Point out every malaria parasite and every leukocyte.
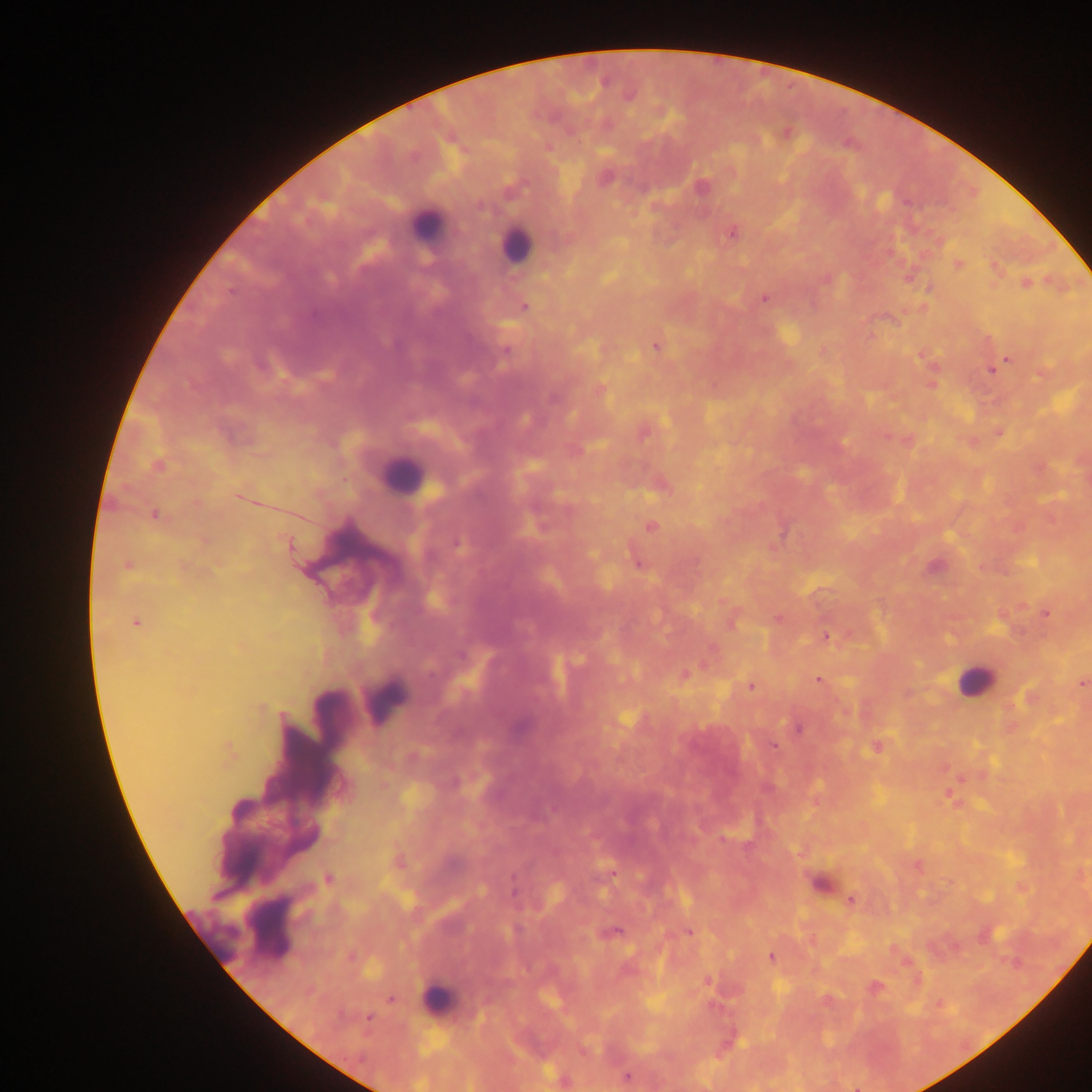
Approximate centers as (x, y) in pixels.
Malaria parasites: (786, 133), (605, 177), (700, 186), (732, 232), (958, 264), (995, 268), (908, 277), (1026, 282), (929, 287), (763, 297), (524, 306), (656, 346), (506, 350), (924, 355), (1007, 358), (993, 370), (931, 383), (599, 389), (643, 430), (999, 431), (969, 441), (157, 466), (660, 485), (239, 496), (155, 514), (651, 527), (457, 543), (637, 561), (128, 565), (1045, 612), (732, 619), (778, 619), (135, 623), (826, 635), (683, 674), (819, 680), (1081, 682), (751, 686), (798, 728), (773, 746), (876, 747), (229, 750), (949, 795), (397, 862), (917, 865), (328, 878), (822, 883), (851, 900), (609, 932), (688, 932), (770, 957), (705, 979), (874, 987), (391, 999), (939, 1003), (368, 1017), (627, 1076), (564, 1080).
Leukocytes: (426, 225), (516, 245), (402, 475), (974, 680), (385, 700), (255, 926), (213, 934), (436, 1000).

image size = 1092×1092 pixels
capture = mobile-phone photograph through a microscope
field of view = single
country = Ghana
preparation = thick blood smear